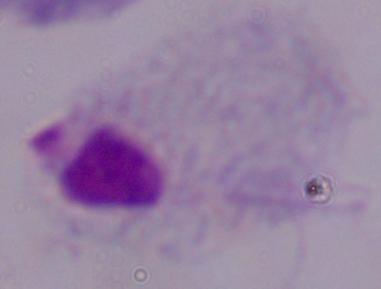
Photomicrograph. 1000x magnification. A trichomonad is seen.